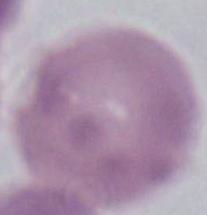
{
  "modality": "micrograph",
  "identification": "erythrocyte",
  "magnification": "1000x"
}